Name the cell type shown.
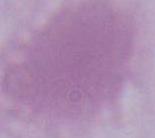
This is an erythrocyte.

Captured at 1000x magnification. Micrograph.